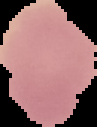
Segmented cell region on a black background. Malaria status: uninfected. Image is 97×127 pixels. From a thin blood film.